Report the malaria status of this cell.
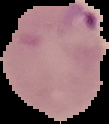
It is parasitized.

The area outside the segmented cell region is set to black. From a thin blood smear. Image is 109×124 pixels.